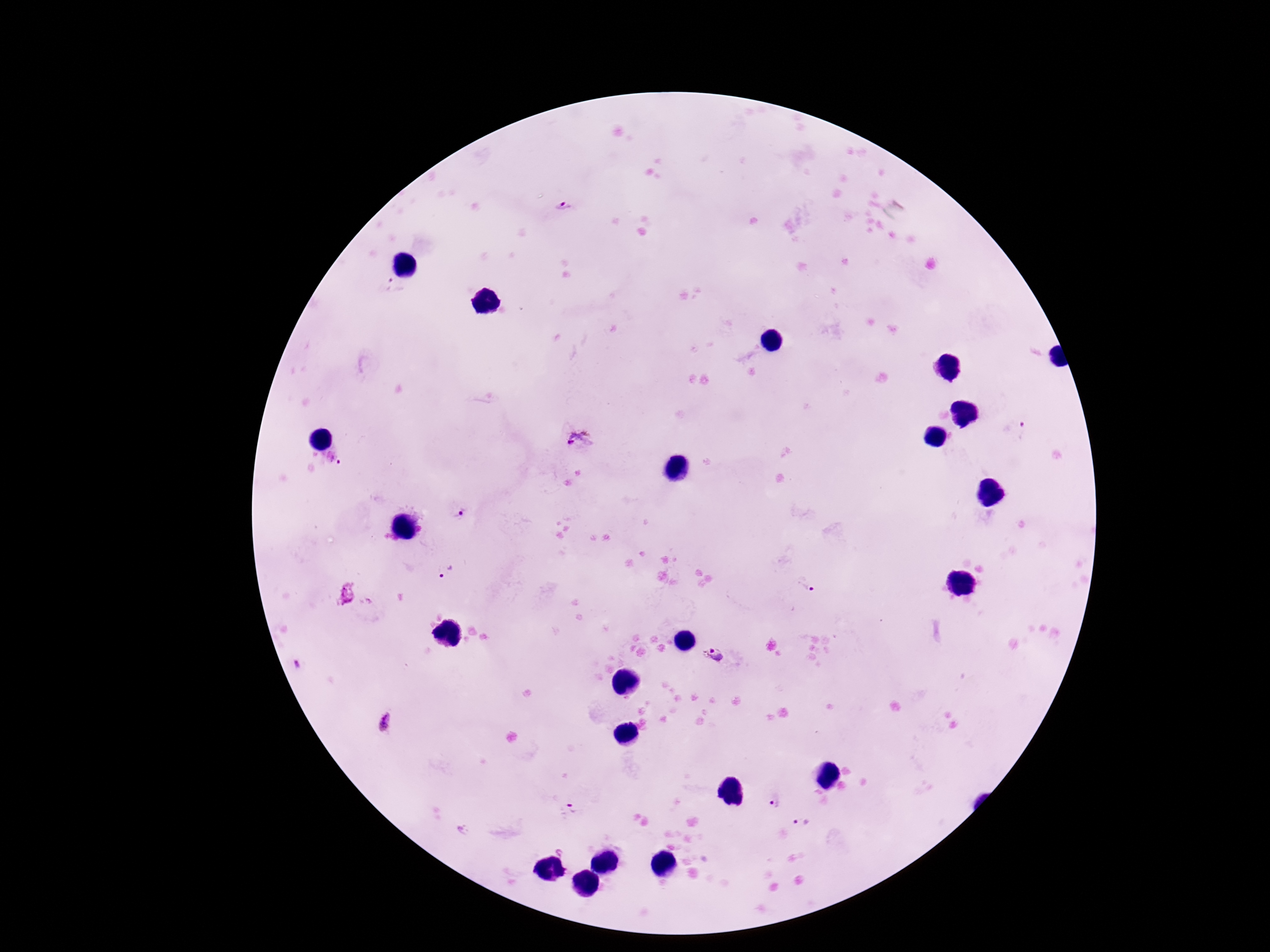 Approximate object centers, in pixels from the top-left corner. Plasmodium parasite locations: (x=564, y=208), (x=393, y=288), (x=1022, y=432), (x=580, y=439), (x=335, y=459), (x=459, y=513), (x=446, y=572), (x=803, y=585), (x=717, y=657), (x=385, y=723), (x=775, y=803), (x=573, y=805), (x=801, y=824). Thick blood film. 100x magnification. Smartphone photograph taken through the microscope eyepiece. One field from this slide. Image is 1270×952 pixels. Giemsa-stained preparation. Patient malaria status: infected.